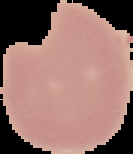

Summary:
  - Image size: 133×154 pixels
  - Malaria status: uninfected
  - Preparation: thin blood film
  - Image type: cell region segmented out of the field of view; surrounding area masked to black